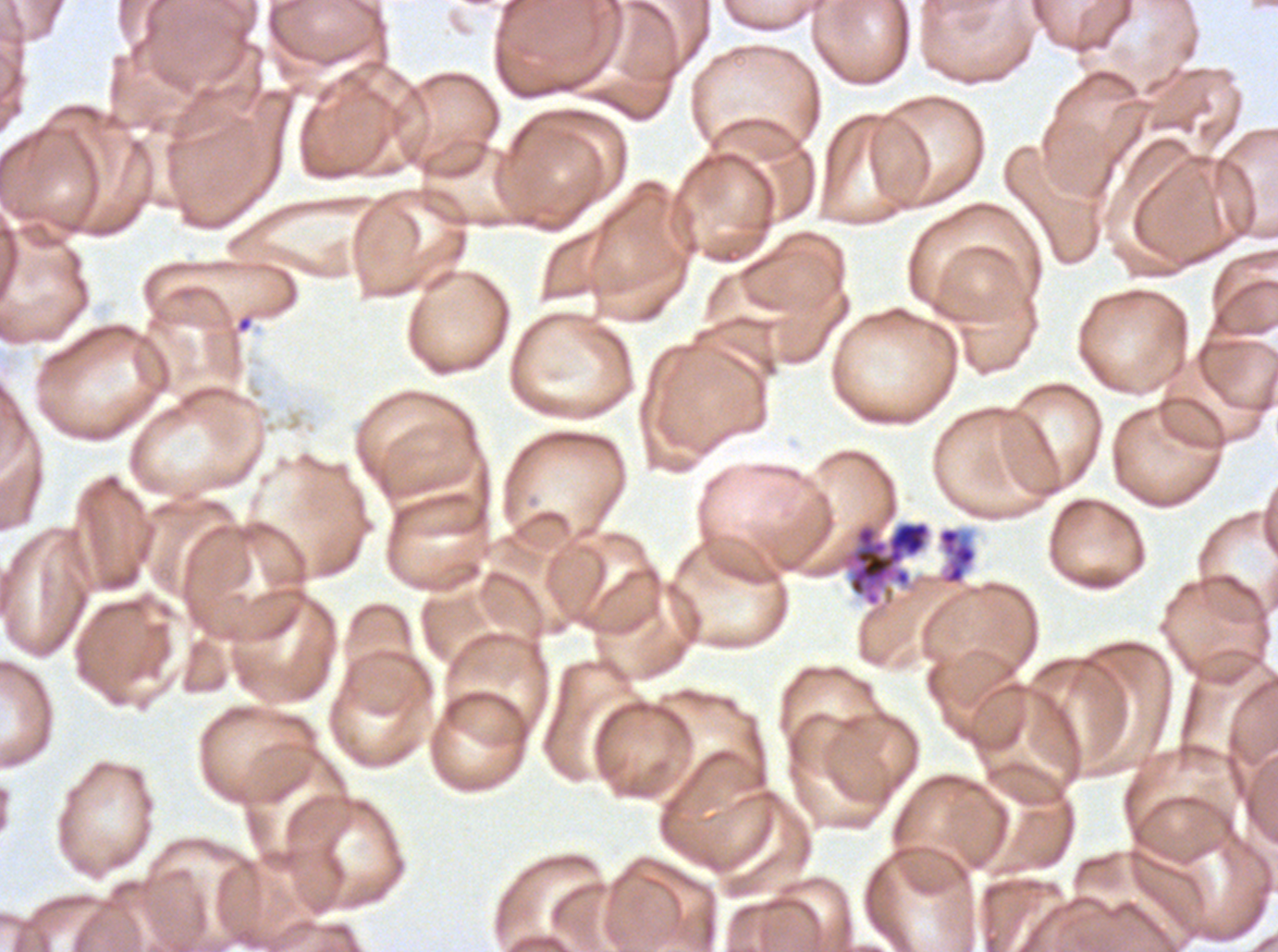
notation = approximate bounding boxes as [x1, y1, x2, y2] in pixels
segmenter locations = [839, 520, 932, 607]
field of view = sub-image separated from a larger composite
stain = Giemsa
preparation = thin blood film
specimen = ex-vivo Plasmodium falciparum culture from a patient in The Gambia, grown for 24 to 48 hours
image size = 1278×952 pixels